Locate every blood parasite and identify its species.
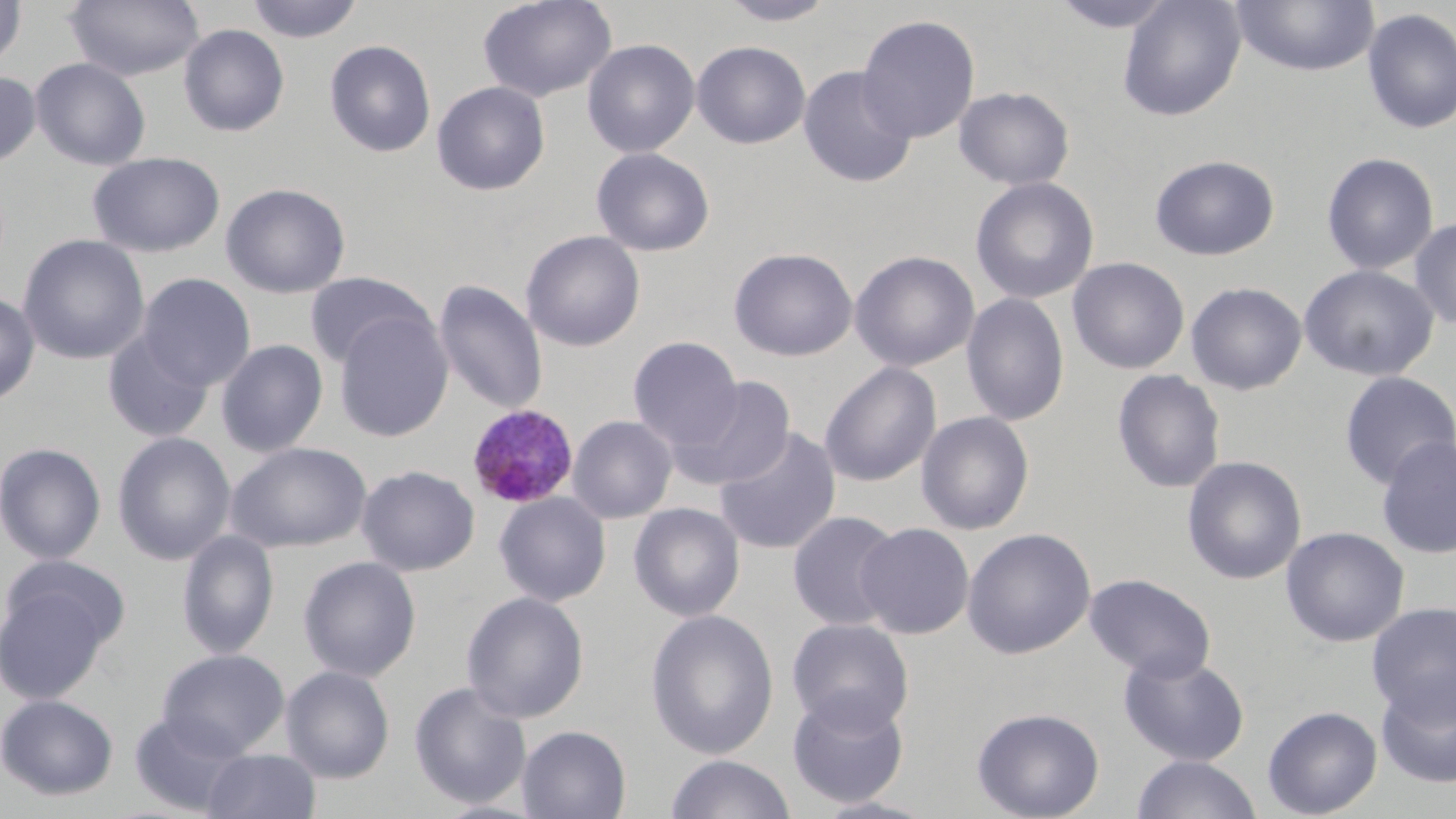
Approximate bounding boxes as [x1, y1, x2, y2] in pixels.
Plasmodium malariae-infected red blood cells: [466, 404, 579, 509].
No Plasmodium falciparum, Plasmodium ovale, Plasmodium vivax, Babesia divergens, or Trypanosoma brucei observed.

Uninfected red blood cell locations: [0, 0, 27, 74], [65, 0, 204, 81], [245, 0, 364, 44], [477, 0, 617, 103], [716, 0, 841, 26], [1049, 0, 1179, 33], [1117, 0, 1246, 121], [1230, 0, 1380, 77], [1361, 7, 1456, 135], [856, 14, 980, 144], [178, 23, 290, 137], [582, 38, 700, 158], [324, 39, 436, 157], [692, 40, 811, 149], [30, 57, 152, 170], [798, 65, 917, 188], [0, 70, 41, 169], [431, 81, 550, 196], [953, 86, 1074, 190], [591, 147, 715, 257], [1320, 151, 1439, 275], [87, 152, 226, 257], [1149, 155, 1280, 261], [970, 177, 1099, 305], [221, 182, 351, 298], [1409, 217, 1456, 330], [520, 230, 646, 352], [18, 234, 150, 365], [729, 247, 858, 362], [849, 250, 980, 372], [1067, 256, 1190, 375], [1298, 264, 1439, 381], [304, 272, 433, 370], [136, 273, 256, 390], [433, 279, 548, 415], [1185, 281, 1307, 395], [0, 291, 40, 406], [961, 293, 1070, 427], [333, 309, 453, 442], [102, 330, 214, 442], [217, 336, 454, 450], [628, 336, 744, 452], [216, 339, 328, 457], [819, 362, 941, 487], [1111, 369, 1226, 494], [1338, 371, 1456, 490], [671, 376, 796, 491], [916, 411, 1034, 535], [567, 415, 678, 523], [714, 426, 842, 555], [112, 431, 236, 565], [1375, 435, 1456, 559], [0, 441, 106, 565], [226, 441, 371, 552], [1182, 455, 1307, 585], [357, 464, 480, 576], [493, 492, 611, 607], [628, 502, 745, 621], [787, 510, 903, 632], [856, 522, 974, 638], [1281, 526, 1409, 647], [962, 527, 1096, 659], [177, 529, 279, 658], [298, 555, 422, 682], [0, 560, 126, 702], [1084, 572, 1215, 682], [461, 590, 590, 724], [1367, 602, 1456, 723], [645, 608, 780, 760], [787, 618, 914, 733], [157, 648, 290, 759], [1118, 651, 1249, 766], [280, 665, 396, 783], [1375, 676, 1456, 789], [408, 681, 532, 810], [787, 692, 911, 809], [0, 694, 119, 801], [1263, 705, 1382, 818], [971, 706, 1105, 819], [128, 710, 250, 816], [517, 724, 631, 819], [202, 748, 321, 819], [664, 754, 797, 818], [1131, 755, 1262, 819], [809, 796, 939, 818]. Slide-level diagnosis: Plasmodium malariae. One field of a larger specimen. Thin blood film. Light microscopy. May-Grünwald-Giemsa stain. Image is 1456×819 pixels. Captured at 1000x magnification.